Outline each Plasmodium malariae-infected red blood cell.
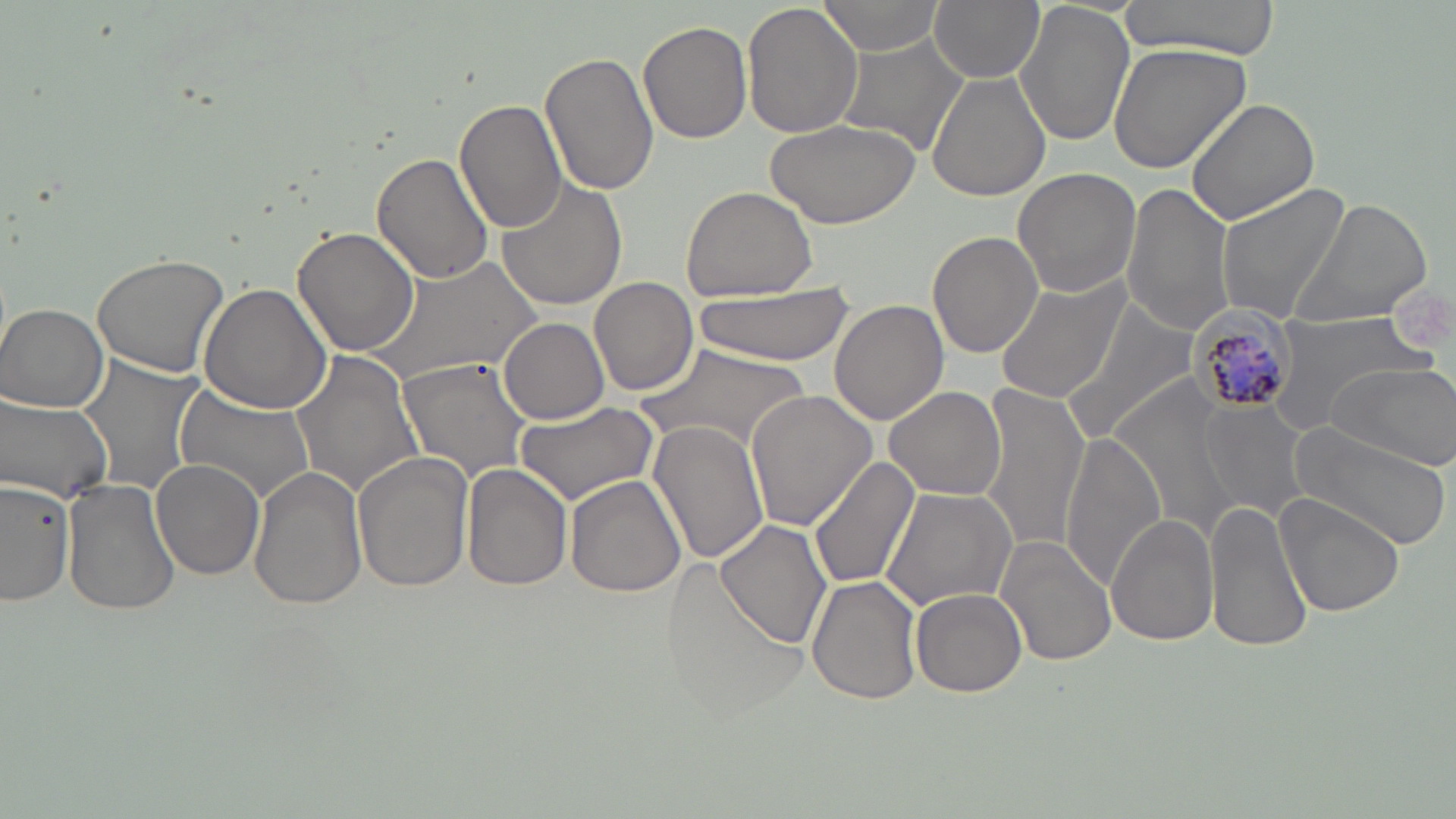

Approximate bounding boxes as (x1, y1, x2, y2) in pixels.
Plasmodium malariae-infected red blood cells: (1184, 299, 1300, 418).

slide-level diagnosis = Plasmodium malariae
magnification = 1000x
uninfected red blood cell locations = approximate bounding boxes as (x1, y1, x2, y2) in pixels: (814, 0, 948, 58), (929, 0, 1043, 82), (1115, 0, 1283, 60), (743, 1, 864, 141), (1014, 3, 1134, 148), (639, 21, 752, 145), (834, 35, 971, 157), (1109, 41, 1249, 175), (540, 49, 657, 197), (928, 71, 1052, 204), (456, 99, 569, 233), (1186, 99, 1321, 223), (766, 115, 922, 231), (371, 151, 493, 285), (1012, 167, 1143, 298), (495, 175, 627, 312), (1121, 182, 1237, 335), (1216, 183, 1350, 324), (680, 185, 818, 301), (1287, 198, 1434, 332), (293, 225, 420, 357), (927, 231, 1043, 359), (91, 252, 230, 379), (359, 259, 547, 384), (589, 276, 700, 398), (995, 276, 1130, 404), (199, 283, 332, 414), (697, 285, 856, 366), (666, 289, 841, 422), (829, 299, 948, 426), (1062, 299, 1201, 441), (1, 303, 109, 411), (1261, 310, 1432, 436), (498, 317, 610, 424), (639, 343, 809, 457), (292, 351, 425, 500), (399, 355, 535, 480), (78, 357, 202, 497), (1323, 361, 1456, 471), (1117, 379, 1248, 542), (173, 381, 318, 507), (974, 384, 1092, 552), (884, 386, 1004, 500), (747, 389, 878, 531), (1, 394, 115, 505), (513, 398, 661, 506), (1197, 399, 1309, 521), (644, 420, 774, 569), (1287, 422, 1452, 553), (1060, 434, 1168, 587), (352, 452, 474, 595), (806, 457, 920, 592), (151, 460, 264, 582), (248, 465, 367, 611), (461, 465, 572, 592), (565, 475, 687, 600), (62, 476, 181, 617), (1, 479, 75, 607), (880, 486, 1017, 611), (1275, 493, 1405, 620), (1206, 500, 1314, 655), (1106, 513, 1219, 647), (717, 518, 833, 648), (996, 537, 1117, 667), (659, 558, 810, 719), (806, 576, 921, 703), (912, 586, 1027, 697)
modality = optical microscopy
image size = 1456×819 pixels
preparation = thin blood smear
stain = May-Grünwald-Giemsa
field of view = single